Point out every Plasmodium parasite.
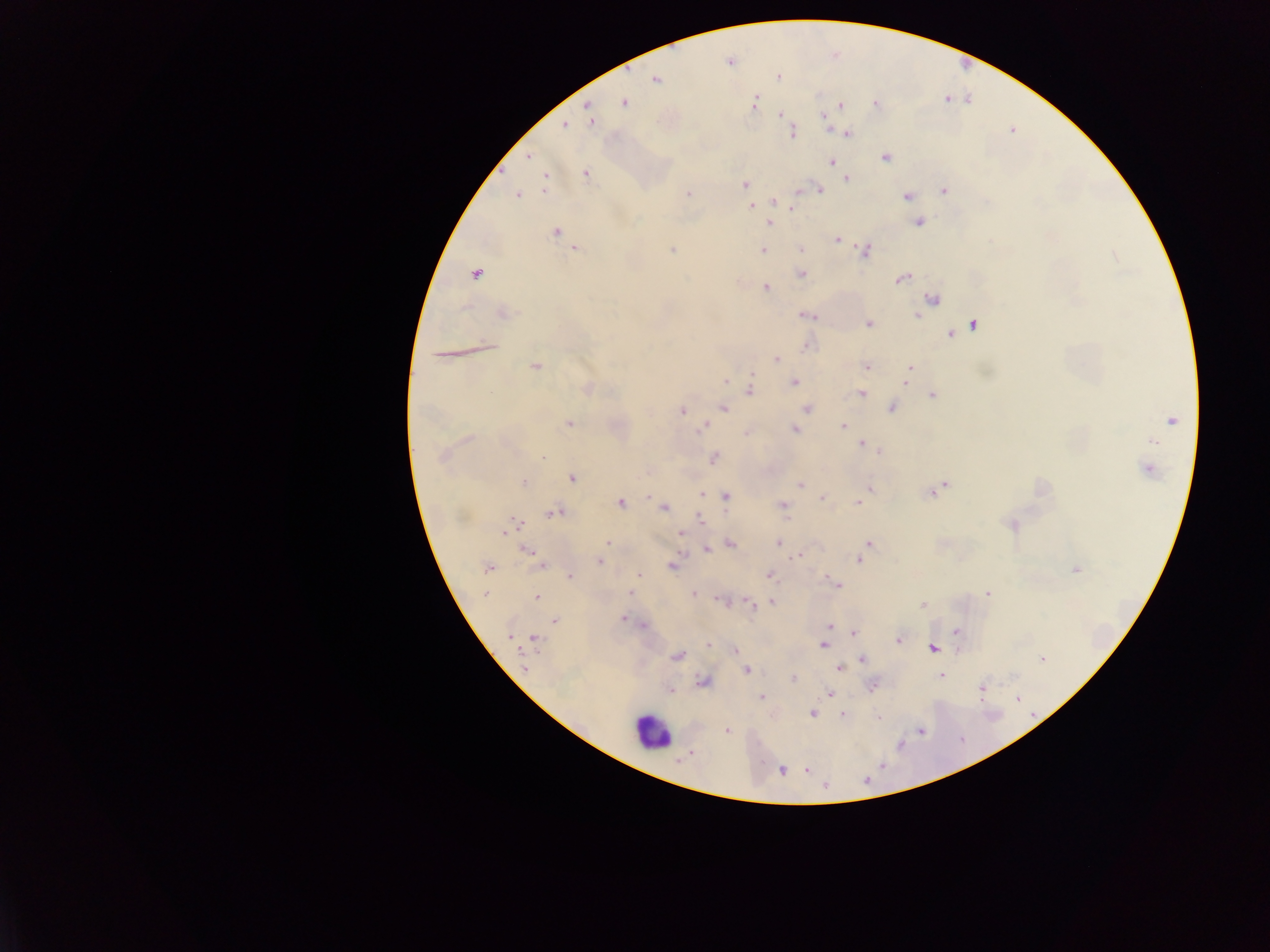
Approximate centers as x y in pixels.
Plasmodium parasites: 656 79; 756 102; 625 103; 584 106; 838 106; 818 115; 823 119; 590 121; 564 124; 792 132; 848 132; 1009 132; 884 156; 526 158; 831 163; 585 172; 846 178; 545 182; 743 184; 543 189; 819 189; 944 189; 688 193; 519 196; 907 196; 773 202; 751 205; 790 209; 918 222; 768 223; 557 231; 836 240; 672 249; 799 249; 574 250; 763 250; 866 251; 801 274; 476 275; 900 279; 765 288; 932 297; 504 312; 916 314; 804 315; 972 323; 866 324; 965 327; 949 334; 489 344; 774 360; 867 367; 535 368; 910 368; 724 381; 794 383; 905 385; 749 387; 589 390; 862 392; 931 394; 723 407; 892 407; 806 408; 682 410; 1172 417; 568 423; 843 425; 704 426; 794 430; 748 433; 861 442; 879 451; 543 457; 713 457; 1145 469; 573 479; 525 482; 948 482; 943 484; 800 485; 869 487; 703 494; 819 494; 930 495; 644 496; 727 496; 822 497; 622 503; 857 503; 781 504; 665 508; 555 512; 698 518; 518 520; 1013 525; 504 534; 681 534; 778 543; 867 543; 608 544; 731 544; 526 550; 706 550; 796 556; 859 560; 599 561; 540 567; 672 567; 487 568; 1074 568; 569 575; 639 576; 769 576; 835 582; 630 591; 693 593; 987 593; 485 595; 535 598; 722 601; 773 601; 749 605; 923 606; 624 618; 641 625; 828 625; 955 631; 853 632; 536 639; 898 639; 707 644; 821 646; 932 648; 735 651; 676 657; 861 659; 1042 659; 839 668; 748 670; 940 676; 794 678; 981 689; 670 692; 828 694; 760 695; 813 714; 842 715; 878 717; 725 730; 781 771.

Leukocyte locations: 652 734. Thick blood film. Single field of view. Image is 1270×952 pixels. Photographed through a microscope with a mobile-phone camera. Collected in Ghana.